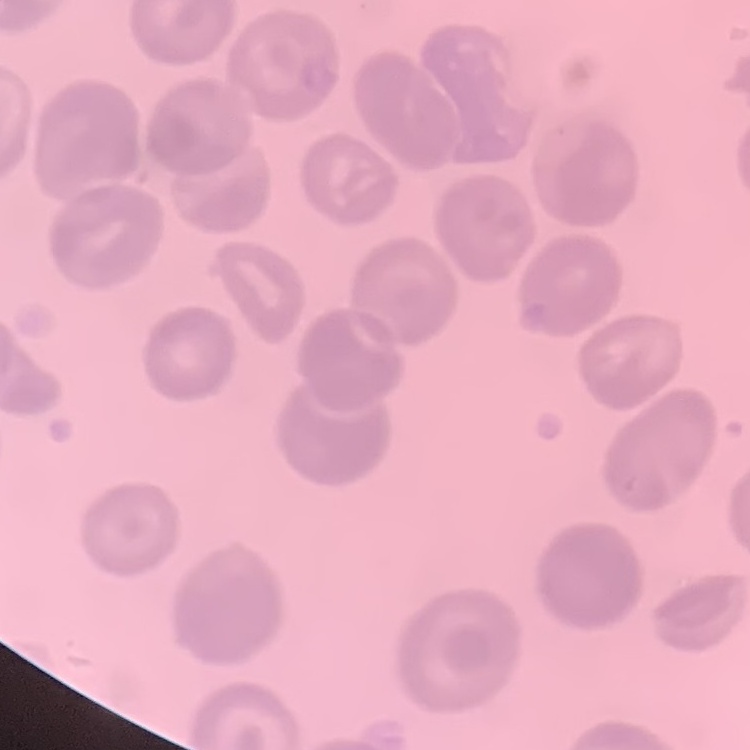 The erythrocytes exhibit no rouleaux formation. Field's or Giemsa stain. One tile cut from a larger photomicrograph. Thin blood film.